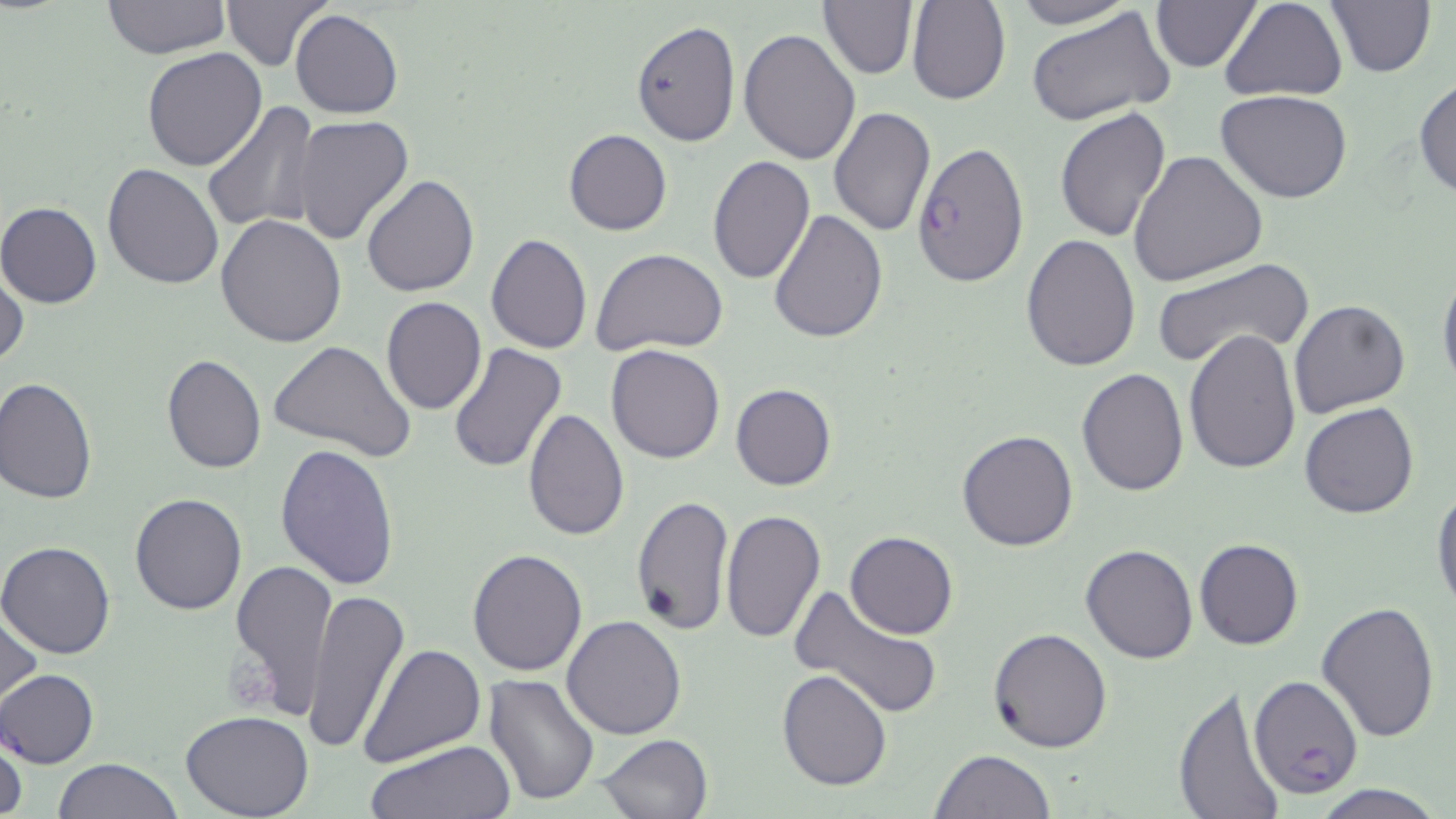

Approximate bounding boxes as [x1, y1, x2, y2] in pixels. Platelet locations: [231, 643, 277, 708]. Plasmodium falciparum-infected red blood cell locations: [912, 141, 1028, 288], [1248, 674, 1364, 800]. Uninfected red blood cell locations: [216, 0, 332, 72], [817, 0, 917, 80], [907, 0, 1011, 105], [1004, 0, 1137, 28], [1219, 0, 1347, 102], [1324, 0, 1435, 77], [100, 1, 232, 57], [1150, 1, 1261, 72], [1026, 6, 1176, 126], [290, 8, 404, 120], [630, 20, 741, 146], [737, 28, 860, 165], [142, 46, 268, 171], [1413, 75, 1456, 201], [1215, 91, 1353, 204], [201, 99, 320, 236], [828, 105, 935, 236], [1053, 108, 1171, 243], [291, 115, 413, 245], [564, 129, 672, 236], [1129, 150, 1266, 288], [706, 155, 814, 284], [102, 164, 223, 289], [361, 173, 481, 297], [0, 202, 102, 308], [768, 210, 888, 342], [216, 213, 348, 347], [486, 233, 592, 355], [1022, 234, 1140, 372], [590, 247, 729, 356], [1151, 257, 1315, 368], [0, 261, 26, 373], [1438, 261, 1456, 400], [382, 297, 486, 415], [1289, 299, 1412, 419], [1185, 328, 1301, 473], [268, 341, 418, 463], [448, 341, 567, 475], [604, 344, 725, 464], [160, 353, 266, 473], [1075, 369, 1188, 496], [0, 379, 99, 504], [730, 383, 837, 491], [1299, 402, 1419, 518], [522, 407, 630, 541], [956, 428, 1078, 551], [275, 441, 400, 589], [1432, 485, 1456, 614], [130, 492, 248, 614], [630, 495, 734, 634], [719, 511, 827, 645], [845, 531, 958, 640], [1195, 539, 1304, 651], [0, 540, 118, 657], [1079, 544, 1199, 664], [467, 548, 588, 677], [228, 558, 338, 720], [791, 586, 944, 720], [302, 587, 409, 760], [1317, 600, 1439, 743], [1, 601, 43, 715], [561, 615, 688, 740], [989, 628, 1111, 753], [360, 644, 487, 767], [359, 660, 590, 789], [777, 668, 891, 790], [0, 669, 100, 768], [483, 674, 601, 808], [1170, 686, 1287, 819], [179, 711, 315, 819], [597, 733, 713, 819], [1, 734, 27, 819], [365, 738, 516, 819], [930, 748, 1056, 818], [54, 758, 184, 819], [1306, 784, 1444, 819]. Slide-level diagnosis: Plasmodium falciparum. May-Grünwald-Giemsa stain. Optical microscopy. Image is 1456×819 pixels. One field of a larger specimen. Captured at 1000x magnification. Thin blood film.